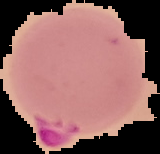

Summary:
  - Result: Plasmodium parasites detected
  - Preparation: thin blood smear
  - Image size: 160×154 pixels
  - Image type: segmented cell region with the area outside set to black